Comment on the morphology of the erythrocytes.
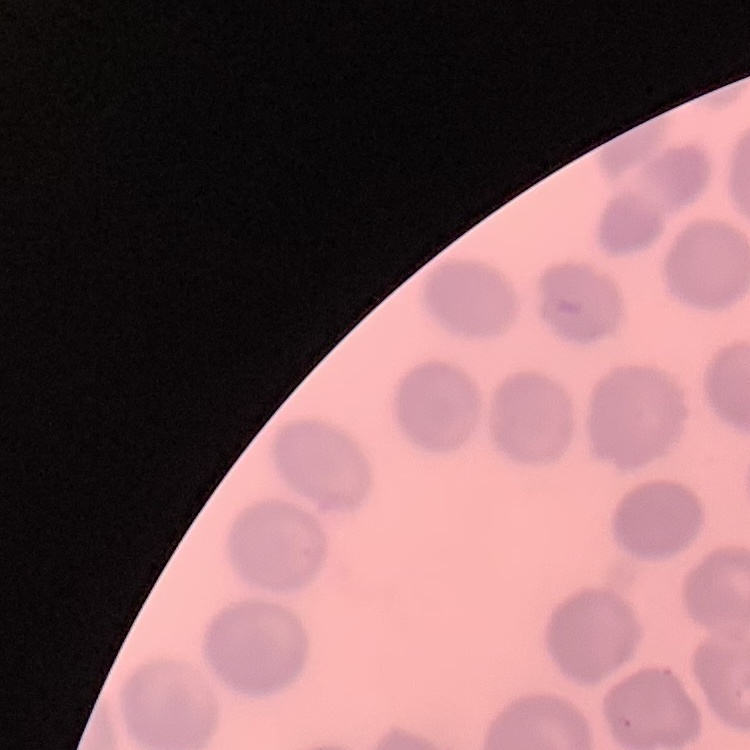

They show no rouleaux formation.

Thin peripheral smear. One tile cut from a larger photomicrograph. Stained with either Field's or Giemsa.